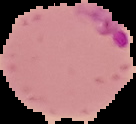

{
  "malaria_status": "parasitized",
  "preparation": "thin blood film",
  "image_type": "segmented cell region on a black background",
  "image_size": "136×124 pixels"
}